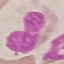

Summary:
  - Result: no malaria parasites detected
  - Image type: cell patch, automatically extracted from a larger field of view and resized to 64 × 64 pixels
  - Preparation: thin smear
  - Capture: smartphone through the microscope eyepiece
  - Stain: Giemsa